Assess the morphology of the red blood cells.
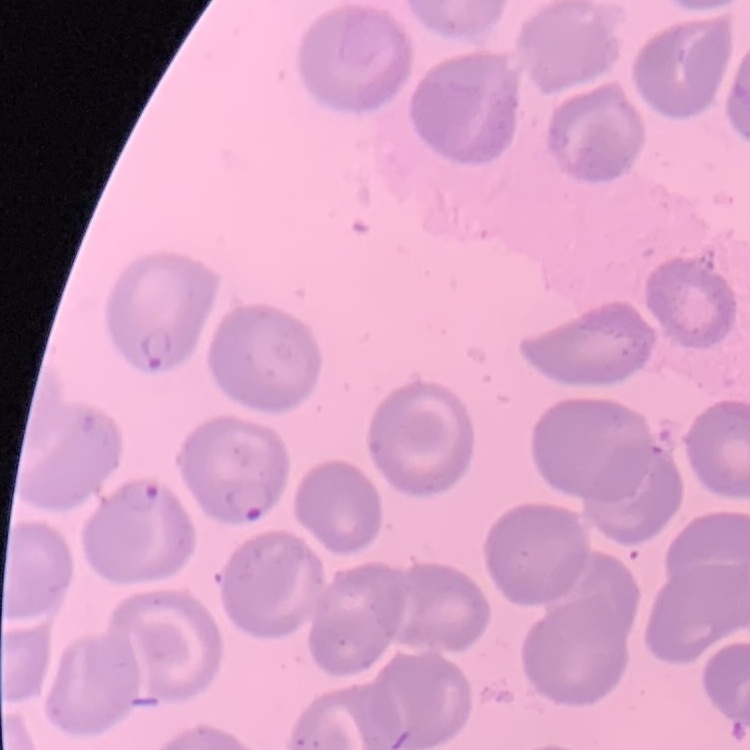
They show no rouleaux formation.

preparation: thin blood film
stain: Field's or Giemsa
image_type: square crop of a larger photomicrograph